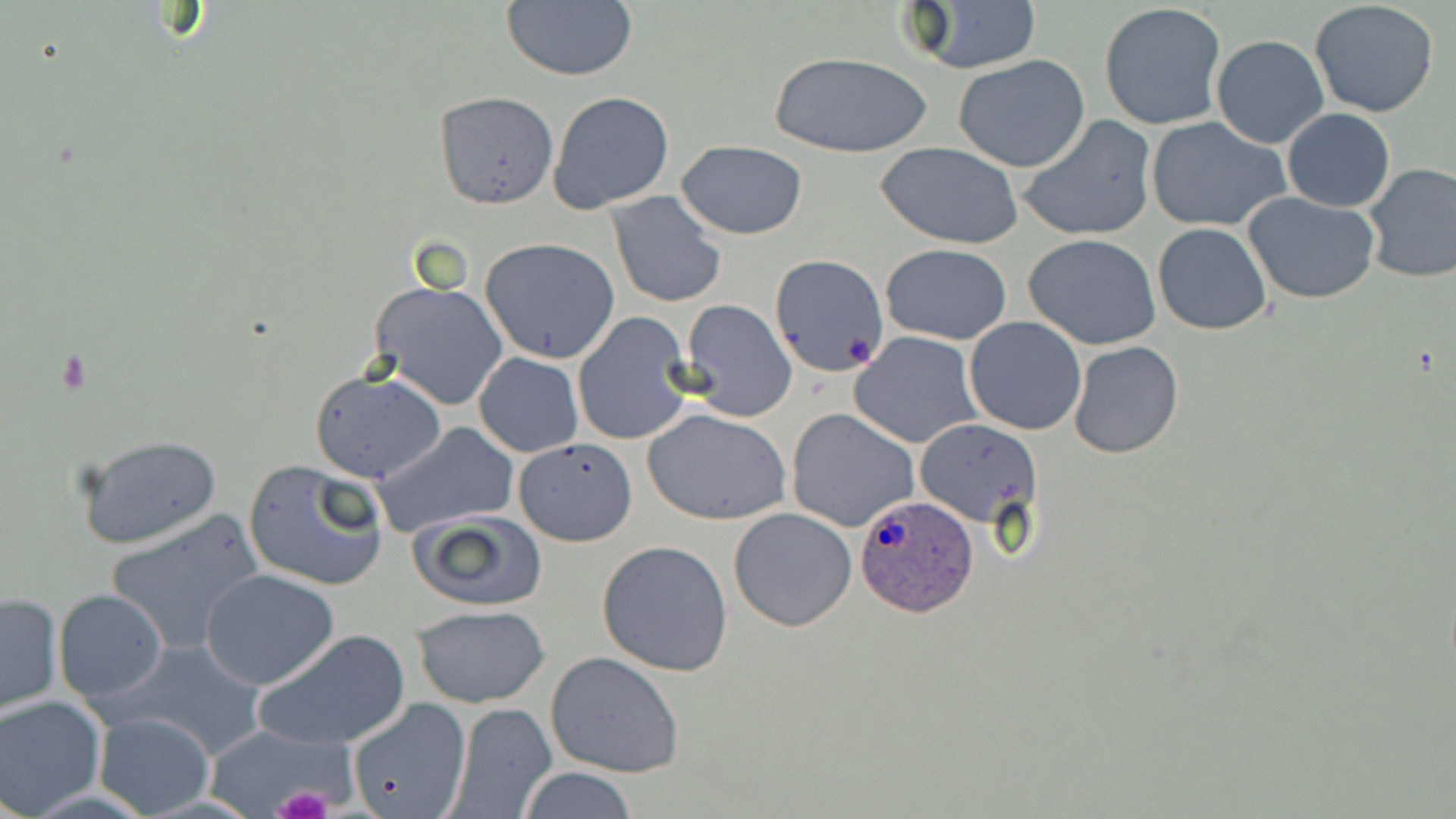

Approximate bounding boxes as (x1,y1)-(x2,y2) corner pairs in pixels. Plasmodium ovale-infected red blood cell locations: (855,494)-(979,617). Uninfected red blood cell locations: (501,0)-(638,82), (902,2)-(1043,75), (1309,2)-(1440,117), (1099,3)-(1226,131), (1211,35)-(1330,150), (771,52)-(931,160), (954,54)-(1089,173), (433,91)-(558,208), (548,91)-(675,213), (1283,109)-(1395,212), (1016,114)-(1157,243), (1146,117)-(1287,232), (676,141)-(808,239), (877,141)-(1026,249), (1362,162)-(1456,283), (605,191)-(726,309), (1243,193)-(1380,305), (1152,223)-(1273,334), (1023,234)-(1164,350), (480,237)-(621,363), (880,244)-(1012,346), (769,253)-(889,378), (370,280)-(509,411), (678,300)-(797,421), (573,314)-(695,445), (965,317)-(1087,436), (850,332)-(982,448), (1068,341)-(1182,459), (474,353)-(583,457), (309,369)-(445,484), (787,408)-(919,532), (644,409)-(790,525), (916,418)-(1040,529), (371,422)-(520,538), (75,432)-(223,550), (516,436)-(638,547), (243,458)-(390,592), (728,507)-(857,630), (106,508)-(264,655), (409,509)-(549,612), (596,539)-(734,675), (202,568)-(339,689), (54,589)-(166,703), (0,591)-(63,715), (413,605)-(548,708), (256,628)-(411,750), (111,639)-(268,760), (545,651)-(684,778), (0,694)-(105,817), (346,701)-(504,819), (446,702)-(557,818), (91,710)-(215,817), (518,766)-(637,819). Platelet locations: (272,785)-(334,819). Slide-level diagnosis: Plasmodium ovale. Light microscopy. 1000x magnification. May-Grünwald-Giemsa stain. Image is 1456×819 pixels. Thin blood film. One field of a larger specimen.